Identify the parasite.
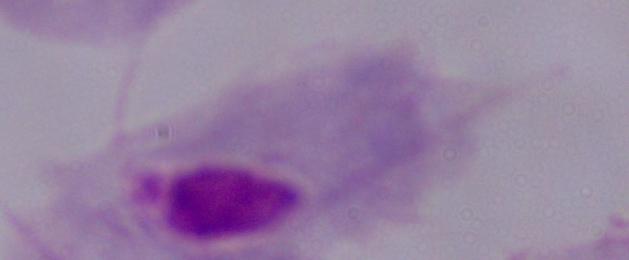
A trichomonad.

magnification = 1000x
modality = micrograph